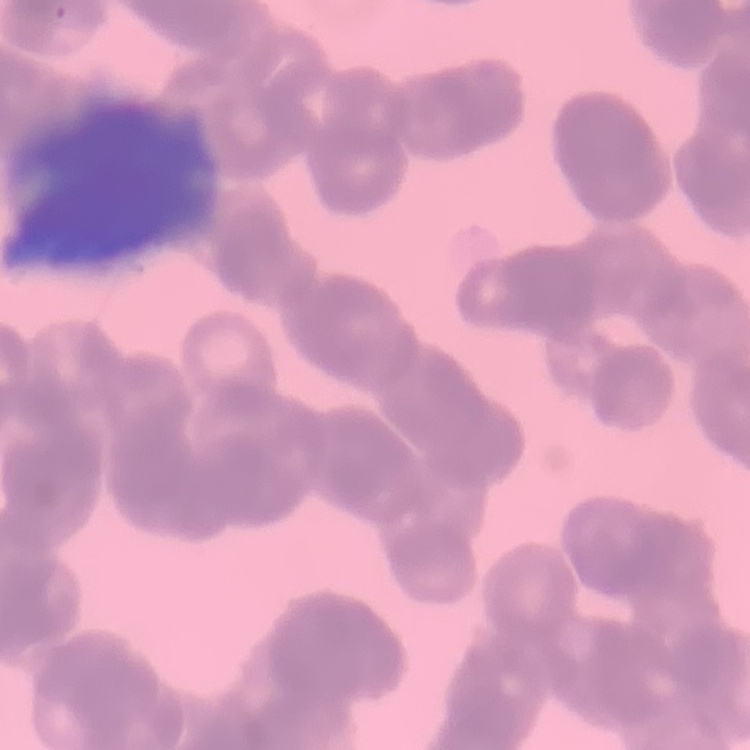
Summary:
  - Erythrocyte morphology: rouleaux formation
  - Stain: Field's or Giemsa
  - Preparation: thin blood film
  - Image type: one tile cut from a larger photomicrograph